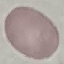
Summary:
  - Malaria status: uninfected
  - Stain: Giemsa
  - Capture: smartphone through the microscope eyepiece
  - Preparation: thin blood film
  - Image type: cell patch, automatically extracted from a larger field of view and resized to 64 × 64 pixels